Classify this cell by malaria status.
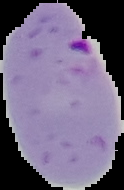
Parasitized.

Summary:
  - Image size: 124×190 pixels
  - Image type: cell region segmented out of the field of view; surrounding area masked to black
  - Preparation: thin blood film